Describe the morphology of the erythrocytes.
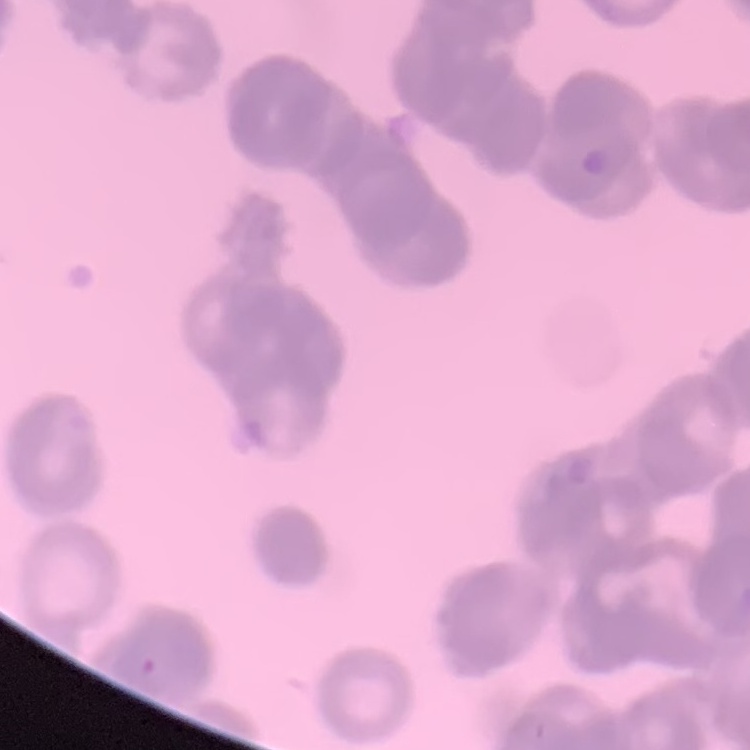

Rouleaux formation.

Stained with either Field's or Giemsa. Square crop of a larger photomicrograph. Thin peripheral smear.